Assess this cell for malaria.
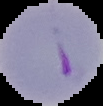

Parasitized.

Summary:
  - Image type: segmented cell region with the area outside set to black
  - Preparation: thin blood smear
  - Image size: 103×106 pixels